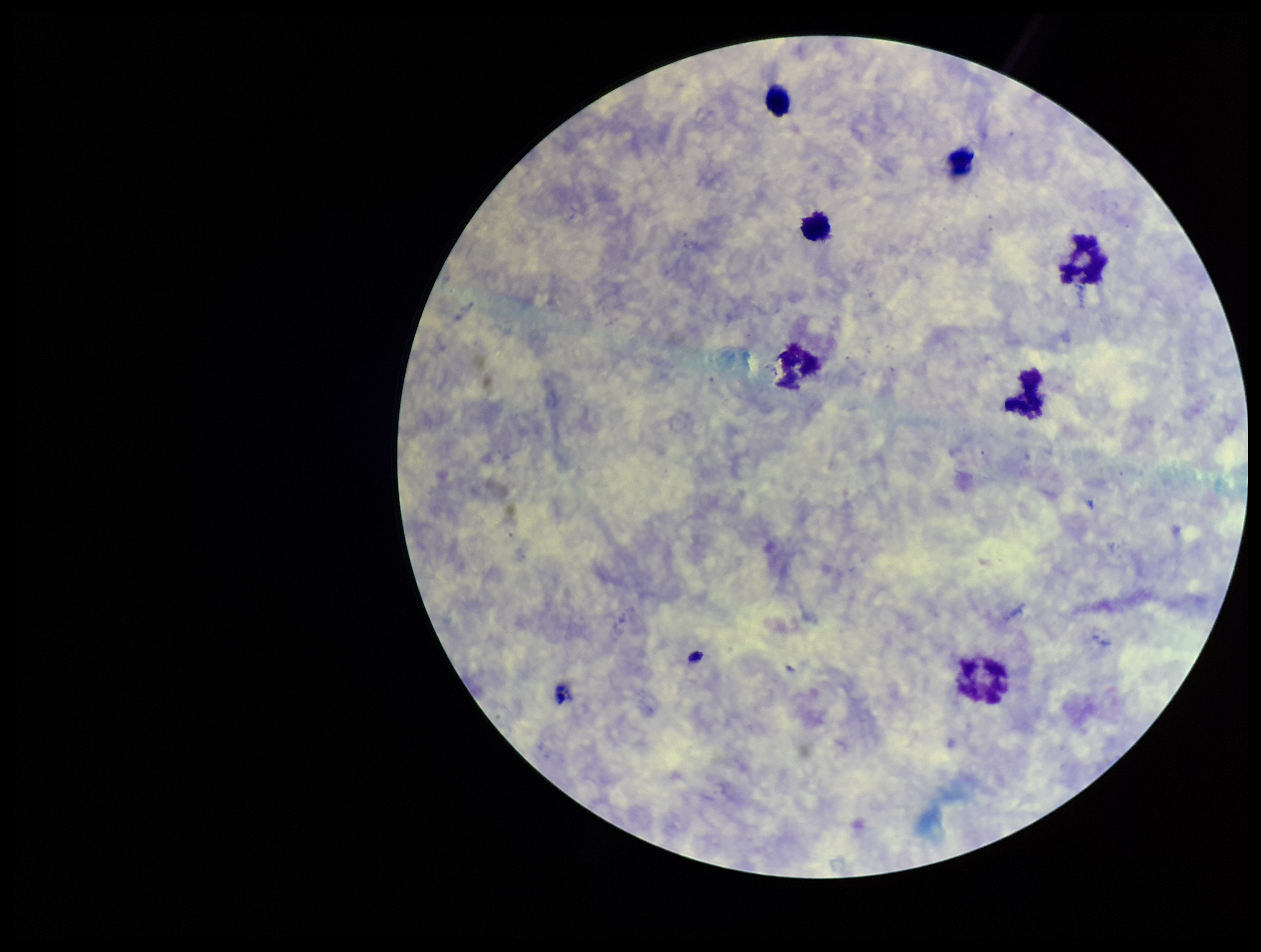 Patient malaria status: negative. Leukocyte count: 7. Preparation: thick smear. One field from this slide. Giemsa stain. Image is 1261×952 pixels. Photographed through the microscope eyepiece with a smartphone camera. Parasite count: 0. Plasmodium parasites: none identified.